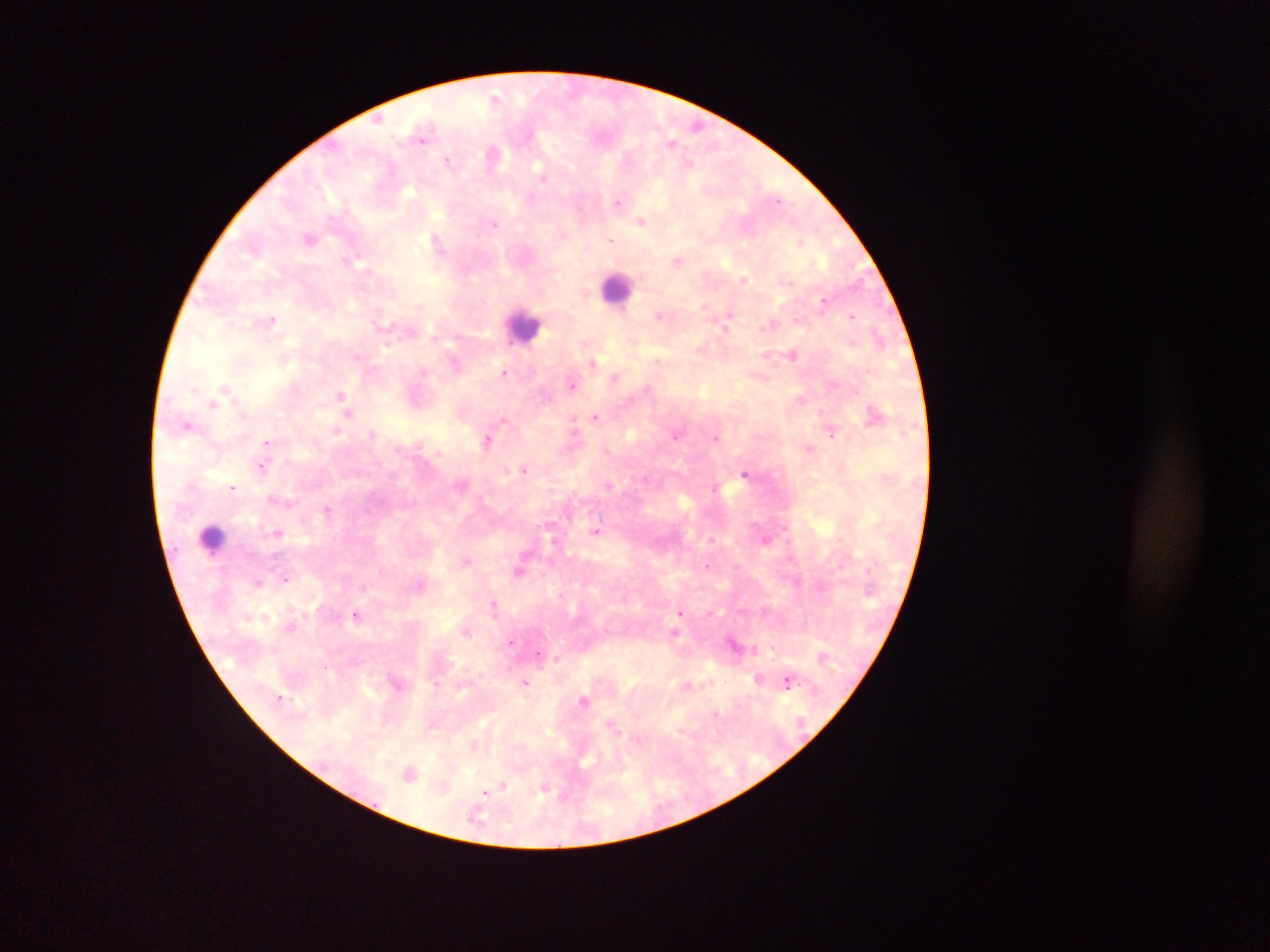 Approximate centers as x y in pixels. Malaria parasite locations: 496 96; 696 126; 423 135; 672 143; 492 153; 449 160; 543 176; 618 202; 642 221; 495 224; 310 238; 438 241; 610 241; 799 241; 678 260; 744 279; 824 299; 660 314; 851 315; 271 319; 726 326; 793 353; 455 362; 592 362; 504 372; 615 377; 573 384; 226 387; 649 389; 341 394; 800 399; 213 403; 348 413; 875 413; 595 417; 188 426; 831 429; 337 430; 372 433; 576 433; 677 435; 717 437; 488 439; 268 442; 810 448; 263 466; 525 469; 745 473; 609 484; 234 486; 273 498; 327 510; 596 531; 277 533; 767 539; 466 559; 709 565; 520 571; 285 577; 798 580; 258 582; 494 606; 680 613; 356 615; 291 626; 467 631; 677 632; 512 640; 735 644; 773 647; 540 654; 556 658; 758 679; 526 681; 788 681; 686 685; 280 697; 584 700; 612 725; 474 744; 410 772; 503 785; 545 787; 486 792. Leukocyte locations: 616 287; 524 325; 213 537. Thick blood smear. Collected in Ghana. Photographed through a microscope with a mobile-phone camera. Single field of view. Image is 1270×952 pixels.